Identify the preparation type.
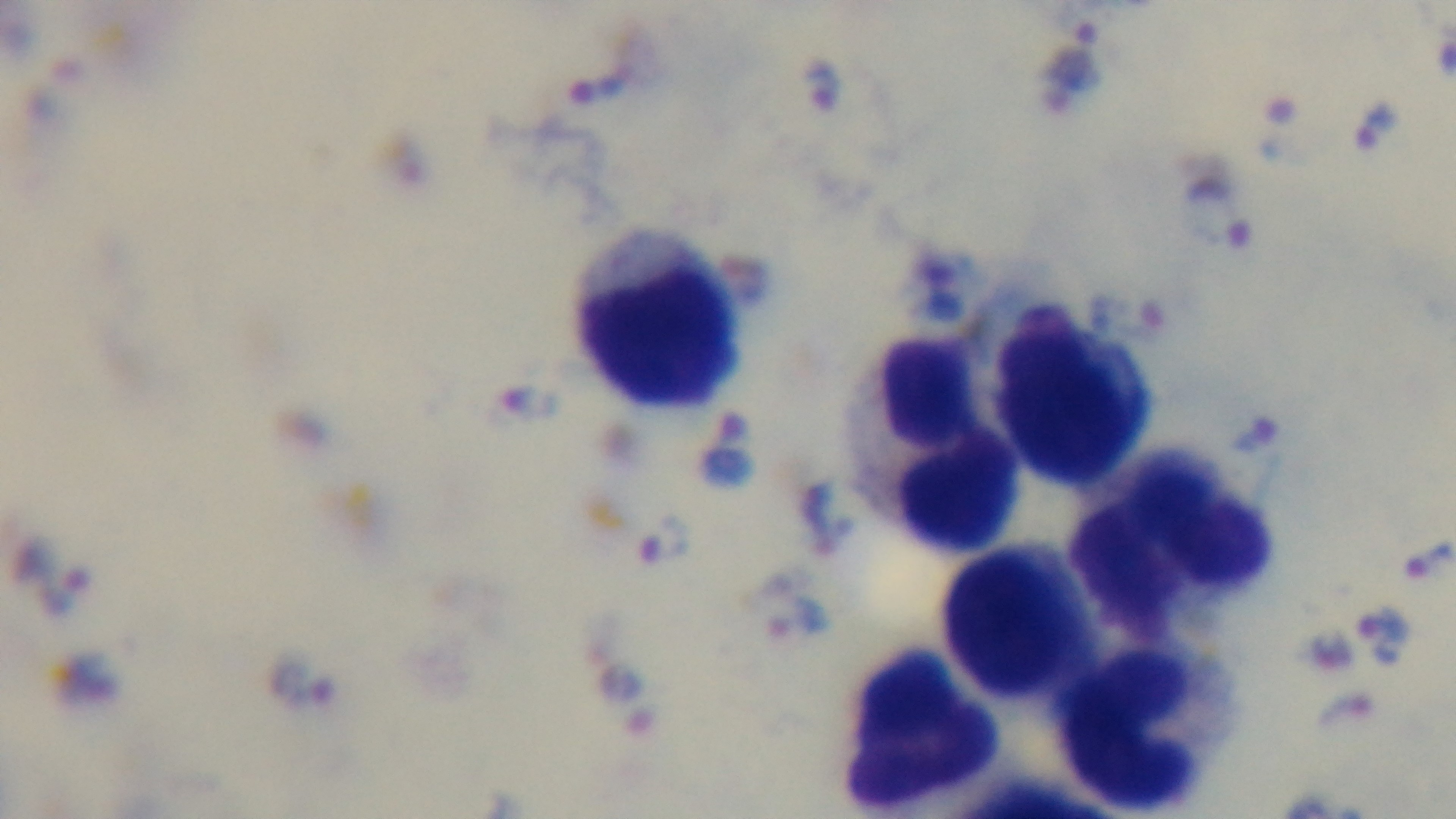

A thick smear.

Summary:
  - Stain: Giemsa
  - Malaria status: infected
  - Modality: light microscopy
  - Objective: 100x oil immersion
  - Capture: mounted 4K digital camera
  - Field of view: one from the slide